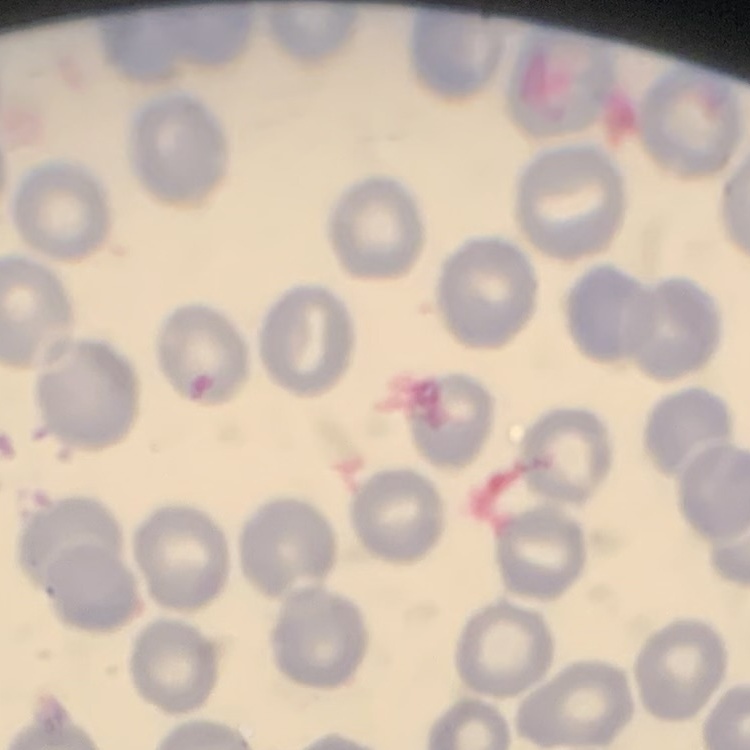

{
  "red_blood_cell_morphology": "no rouleaux formation",
  "preparation": "thin peripheral smear",
  "image_type": "square crop of a larger photomicrograph",
  "stain": "Field's or Giemsa"
}